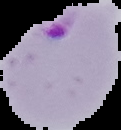

Malaria status: parasitized. Image is 121×130 pixels. The area outside the segmented cell region is set to black. From a thin blood film.